Identify the blood parasite species.
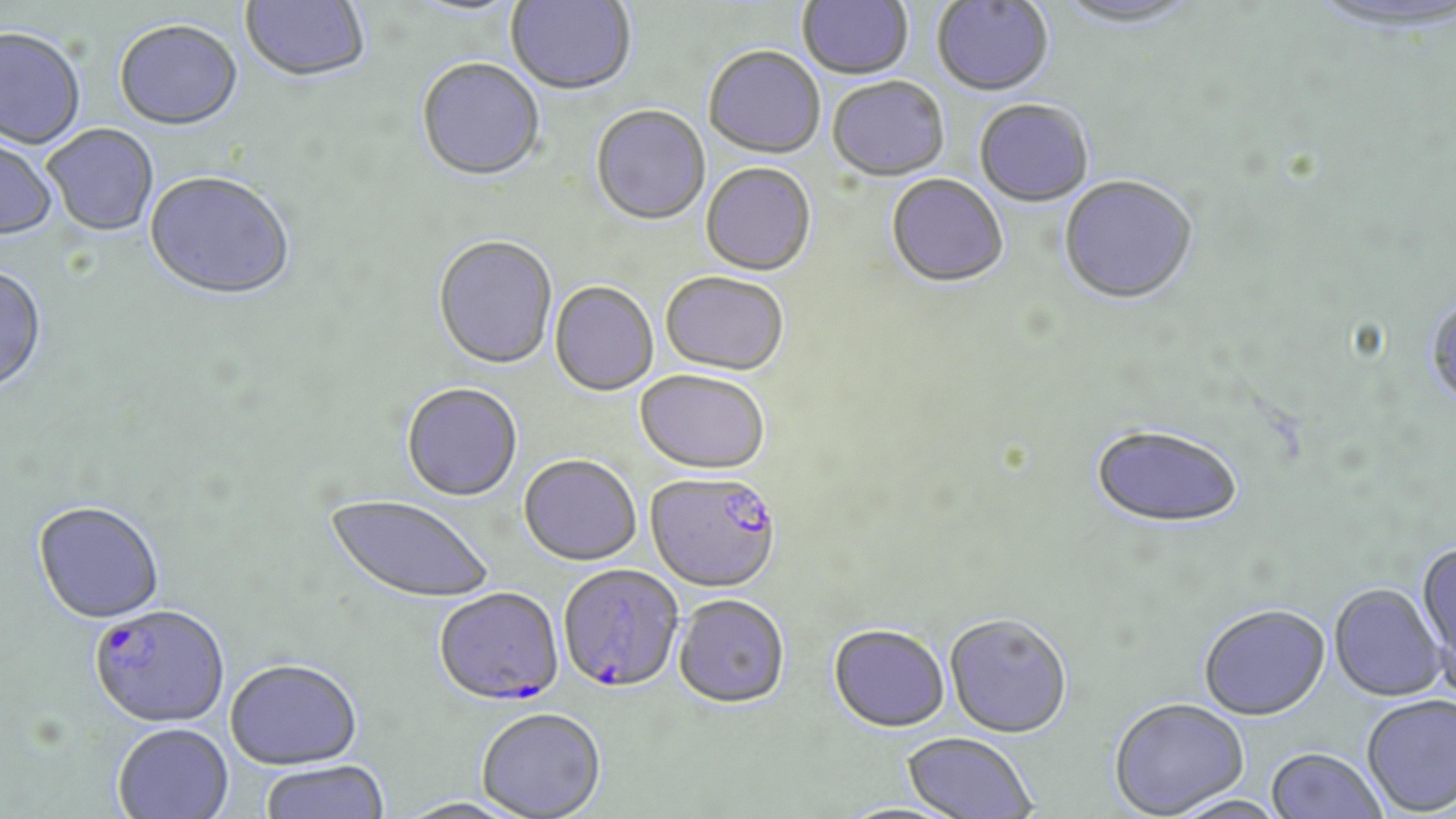

Plasmodium falciparum.

Summary:
  - Coordinate format: approximate bounding boxes as named x1/y1/x2/y2 corners in pixels
  - Uninfected red blood cell locations: (x1=240, y1=0, x2=371, y2=86), (x1=506, y1=0, x2=636, y2=97), (x1=798, y1=0, x2=913, y2=81), (x1=1304, y1=0, x2=1453, y2=34), (x1=406, y1=1, x2=527, y2=20), (x1=932, y1=1, x2=1054, y2=99), (x1=1053, y1=1, x2=1202, y2=31), (x1=114, y1=22, x2=243, y2=133), (x1=0, y1=29, x2=86, y2=151), (x1=703, y1=48, x2=826, y2=160), (x1=416, y1=60, x2=545, y2=184), (x1=827, y1=79, x2=950, y2=182), (x1=975, y1=101, x2=1093, y2=208), (x1=590, y1=107, x2=711, y2=227), (x1=43, y1=126, x2=159, y2=237), (x1=0, y1=134, x2=59, y2=241), (x1=701, y1=164, x2=816, y2=277), (x1=144, y1=174, x2=296, y2=304), (x1=886, y1=176, x2=1009, y2=290), (x1=1059, y1=177, x2=1199, y2=307), (x1=433, y1=237, x2=558, y2=371), (x1=0, y1=267, x2=48, y2=396), (x1=660, y1=273, x2=789, y2=377), (x1=550, y1=282, x2=658, y2=397), (x1=1425, y1=294, x2=1456, y2=410), (x1=635, y1=371, x2=770, y2=476), (x1=401, y1=383, x2=522, y2=503), (x1=1090, y1=423, x2=1245, y2=530), (x1=518, y1=455, x2=641, y2=566), (x1=325, y1=494, x2=494, y2=605), (x1=33, y1=503, x2=165, y2=626), (x1=1414, y1=541, x2=1456, y2=691), (x1=1329, y1=583, x2=1447, y2=701), (x1=673, y1=594, x2=790, y2=708), (x1=1199, y1=603, x2=1330, y2=719), (x1=944, y1=614, x2=1072, y2=738), (x1=828, y1=623, x2=950, y2=732), (x1=224, y1=658, x2=363, y2=769), (x1=1361, y1=694, x2=1456, y2=816), (x1=1109, y1=697, x2=1249, y2=818), (x1=476, y1=708, x2=606, y2=818), (x1=112, y1=723, x2=234, y2=819), (x1=901, y1=732, x2=1037, y2=819), (x1=1266, y1=746, x2=1388, y2=819), (x1=259, y1=760, x2=391, y2=819), (x1=395, y1=797, x2=528, y2=819)
  - Plasmodium falciparum-infected red blood cell locations: (x1=646, y1=470, x2=783, y2=593), (x1=558, y1=564, x2=683, y2=693), (x1=434, y1=588, x2=564, y2=707), (x1=89, y1=606, x2=230, y2=729)
  - Field of view: one of a larger specimen
  - Magnification: 1000x
  - Stain: May-Grünwald-Giemsa
  - Preparation: thin blood film
  - Image size: 1456×819 pixels
  - Modality: light microscopy